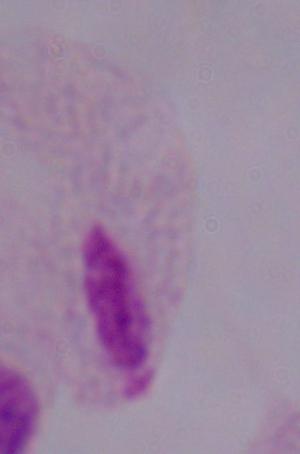
Summary:
  - Identification: trichomonad
  - Magnification: 1000x
  - Modality: micrograph